Assess this cell for malaria.
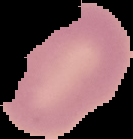

Uninfected.

Segmented cell region on a black background. Image is 133×139 pixels. From a thin blood film.